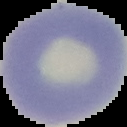
Summary:
  - Image type: segmented cell region with the area outside set to black
  - Image size: 127×127 pixels
  - Result: negative for Plasmodium parasites
  - Preparation: thin blood smear